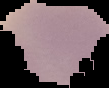

From a thin blood smear. Cell region segmented out of the field of view; the surrounding area is masked to black. Result: no Plasmodium parasites detected. Image is 109×88 pixels.